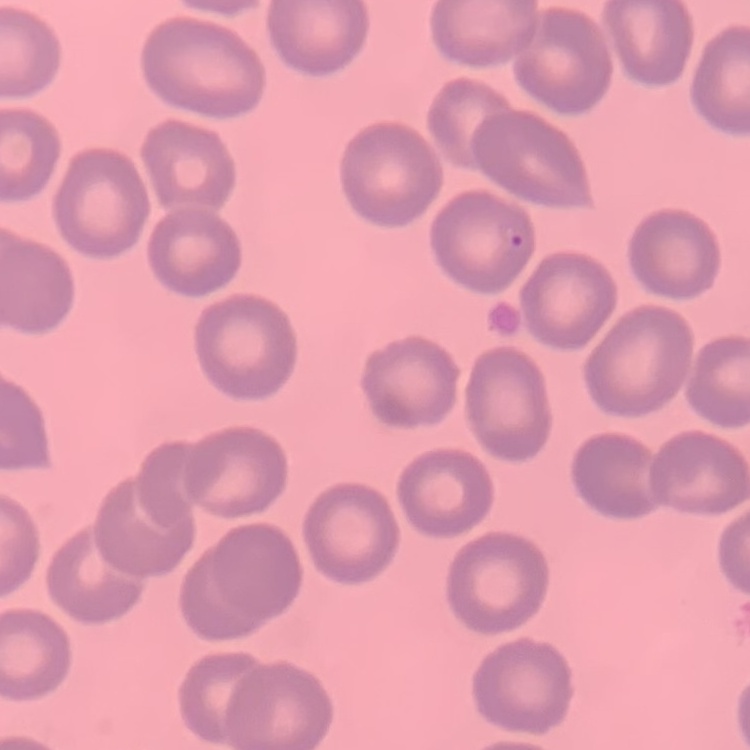
Summary:
  - Erythrocyte morphology: no rouleaux formation
  - Image type: one tile cut from a larger photomicrograph
  - Stain: Field's or Giemsa
  - Preparation: thin blood film